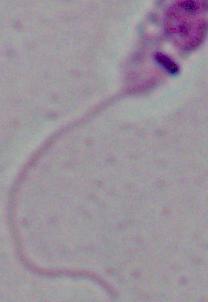
Summary:
  - Magnification: 1000x
  - Modality: micrograph
  - Identification: Leishmania